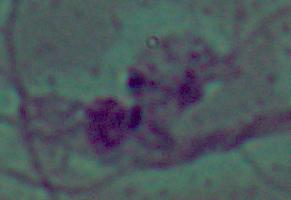
Summary:
  - Identification: Leishmania
  - Modality: micrograph
  - Magnification: 1000x